Classify this cell by malaria status.
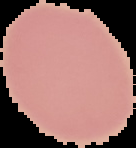
It is uninfected.

image type = segmented cell region on a black background
image size = 136×148 pixels
preparation = thin blood film